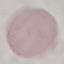 Malaria status: uninfected. Acquired by smartphone through the microscope eyepiece. Thin blood film. Giemsa-stained preparation. Cell patch, automatically extracted from a larger field of view and resized to 64 × 64 pixels.